State which parasite is depicted.
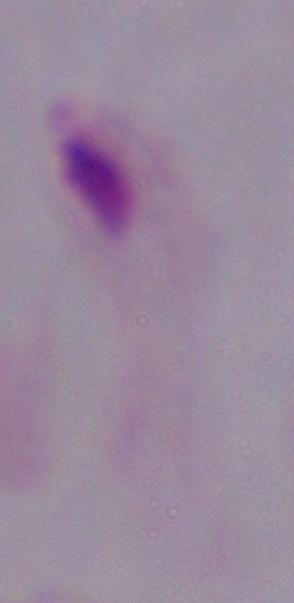
A trichomonad.

Summary:
  - Modality: micrograph
  - Magnification: 1000x